Comment on the morphology of the red blood cells.
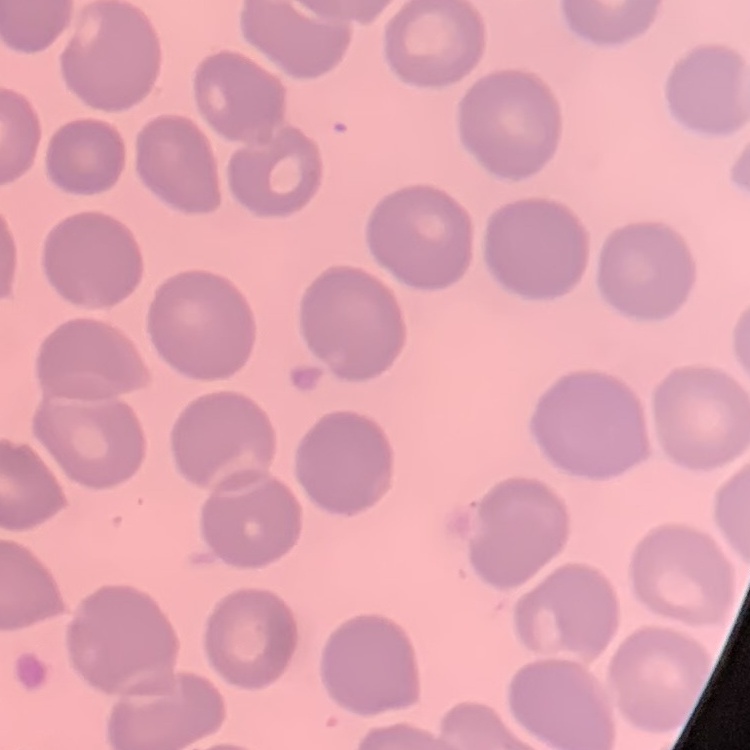
They show no rouleaux formation.

Summary:
  - Image type: square crop of a larger photomicrograph
  - Preparation: thin blood film
  - Stain: Field's or Giemsa